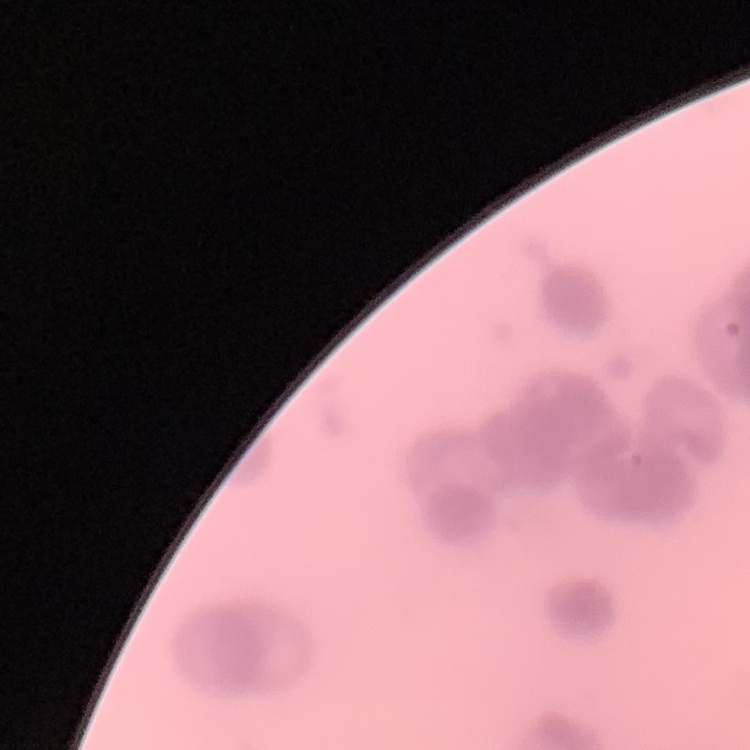
Summary:
  - Red blood cell morphology: rouleaux formation
  - Preparation: thin blood film
  - Image type: one tile cut from a larger photomicrograph
  - Stain: Field's or Giemsa